State the blood parasite species.
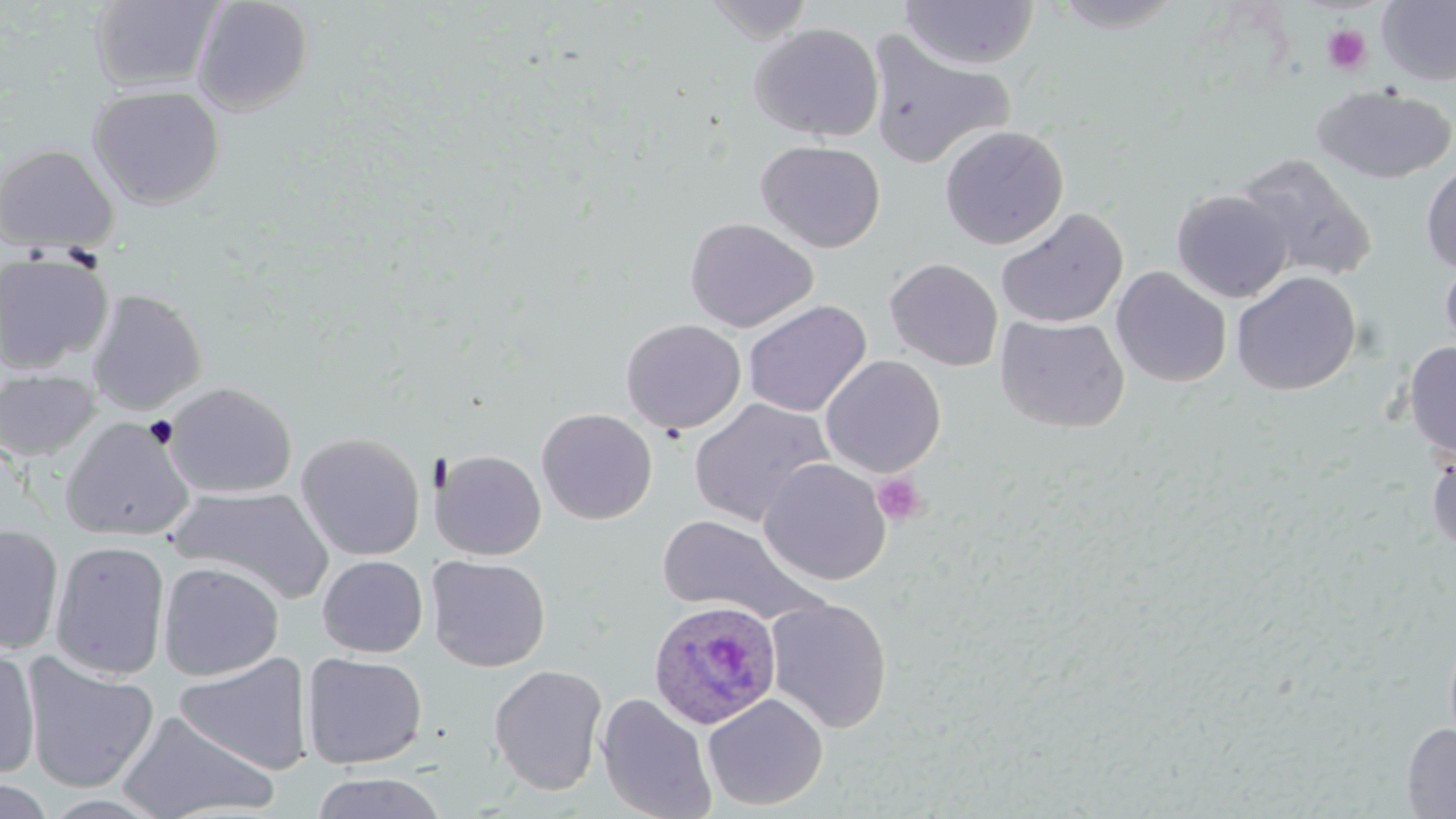

Plasmodium ovale.

Approximate bounding boxes as (x1, y1, x2, y2) in pixels. Platelet locations: (1321, 24, 1373, 77), (871, 473, 927, 526). Plasmodium ovale-infected red blood cell locations: (649, 599, 781, 729). Uninfected red blood cell locations: (192, 0, 314, 115), (703, 0, 820, 44), (1377, 0, 1456, 86), (90, 1, 224, 93), (900, 1, 1039, 70), (1045, 1, 1191, 33), (749, 23, 884, 141), (863, 28, 1016, 171), (87, 84, 225, 210), (1312, 84, 1455, 184), (939, 125, 1068, 249), (755, 140, 885, 253), (0, 143, 119, 254), (1234, 152, 1378, 283), (1421, 162, 1456, 273), (1171, 189, 1293, 302), (996, 208, 1128, 330), (685, 217, 818, 333), (0, 251, 114, 373), (1439, 254, 1456, 360), (885, 258, 1003, 371), (1110, 266, 1232, 387), (1230, 271, 1361, 395), (86, 288, 208, 415), (742, 299, 872, 417), (994, 315, 1129, 433), (620, 318, 746, 434), (1402, 341, 1456, 459), (820, 354, 946, 478), (0, 369, 100, 462), (164, 381, 297, 499), (688, 398, 834, 528), (536, 407, 658, 524), (59, 416, 195, 541), (295, 432, 426, 561), (1426, 447, 1456, 555), (432, 450, 546, 560), (758, 458, 891, 586), (169, 485, 333, 604), (655, 514, 829, 626), (0, 523, 64, 655), (50, 539, 171, 681), (317, 554, 428, 657), (426, 554, 550, 672), (157, 561, 284, 681), (765, 597, 893, 734), (0, 646, 41, 780), (301, 652, 428, 770), (22, 653, 159, 794), (174, 653, 313, 774), (488, 664, 609, 796), (702, 692, 829, 811), (595, 693, 717, 819), (115, 708, 278, 819), (1401, 723, 1456, 818), (309, 772, 449, 819), (0, 776, 57, 818). May-Grünwald-Giemsa-stained preparation. Image is 1456×819 pixels. 1000x magnification. Thin blood film. Single field of view. Optical microscopy.